Locate every blood parasite and identify its species.
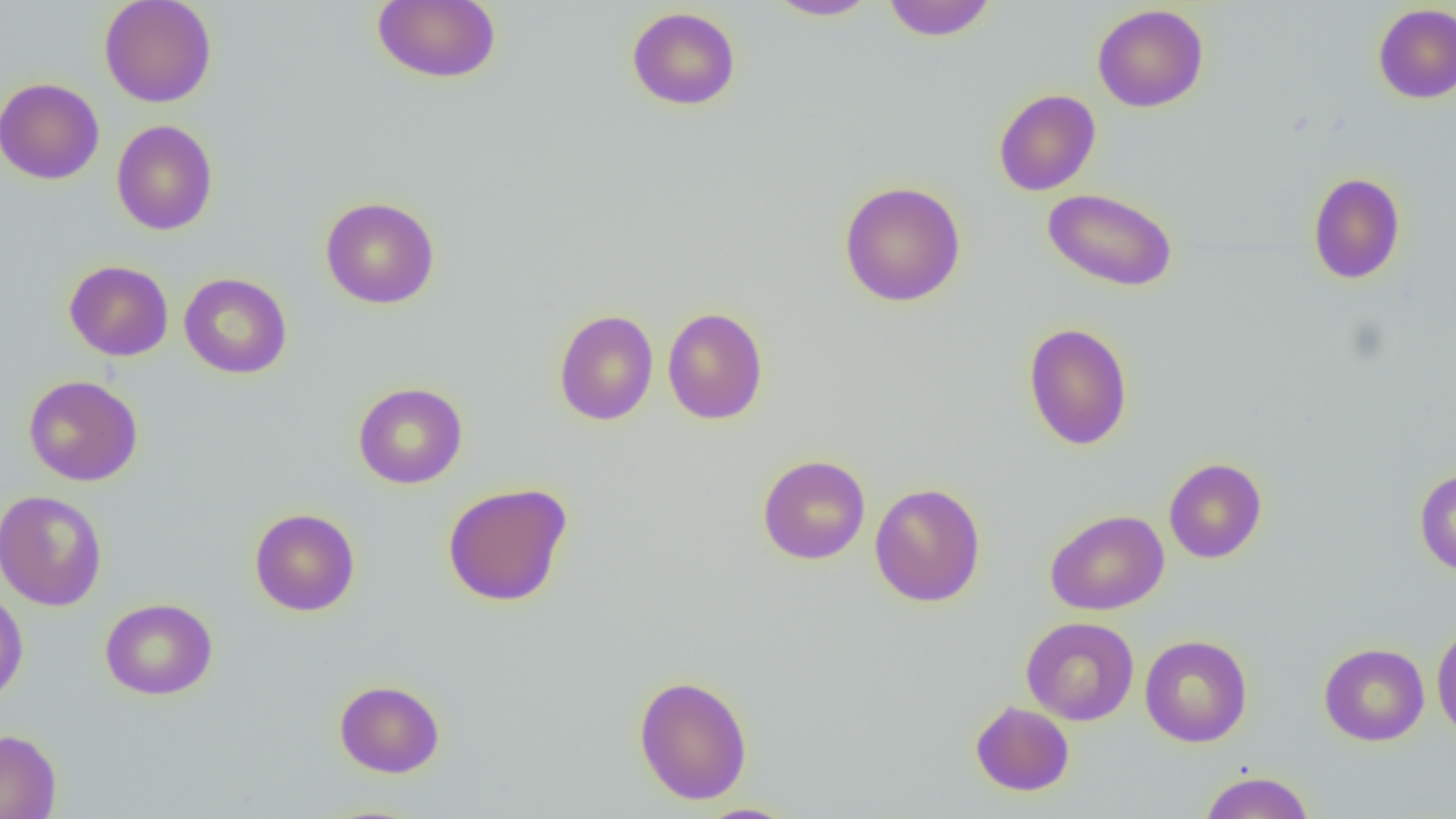
No blood parasites observed.

Approximate bounding boxes as [x1, y1, x2, y2] in pixels. Uninfected red blood cell locations: [99, 0, 218, 107], [372, 0, 501, 84], [765, 0, 882, 21], [880, 0, 998, 42], [1372, 3, 1456, 104], [1092, 4, 1209, 113], [627, 6, 741, 110], [0, 78, 104, 184], [993, 89, 1101, 196], [111, 120, 218, 236], [1307, 172, 1406, 284], [839, 181, 966, 306], [1042, 187, 1178, 292], [320, 196, 440, 309], [64, 260, 174, 361], [63, 266, 292, 365], [179, 272, 292, 379], [662, 307, 768, 424], [554, 309, 658, 425], [1023, 322, 1133, 451], [23, 374, 143, 486], [353, 382, 467, 489], [757, 454, 870, 564], [1163, 457, 1267, 563], [1413, 468, 1456, 577], [442, 482, 573, 607], [869, 482, 985, 607], [1, 489, 107, 611], [249, 508, 360, 616], [1045, 509, 1169, 615], [0, 588, 28, 708], [100, 598, 218, 700], [1021, 616, 1139, 725], [1431, 622, 1456, 742], [1140, 634, 1253, 747], [1319, 642, 1430, 746], [633, 674, 752, 804], [334, 679, 445, 778], [970, 701, 1075, 796], [0, 729, 61, 819], [1198, 770, 1314, 818], [694, 803, 802, 819]. Slide-level diagnosis: negative for blood parasites. Image is 1456×819 pixels. Captured at 1000x magnification. Light microscopy. Single field of view. Thin blood smear.